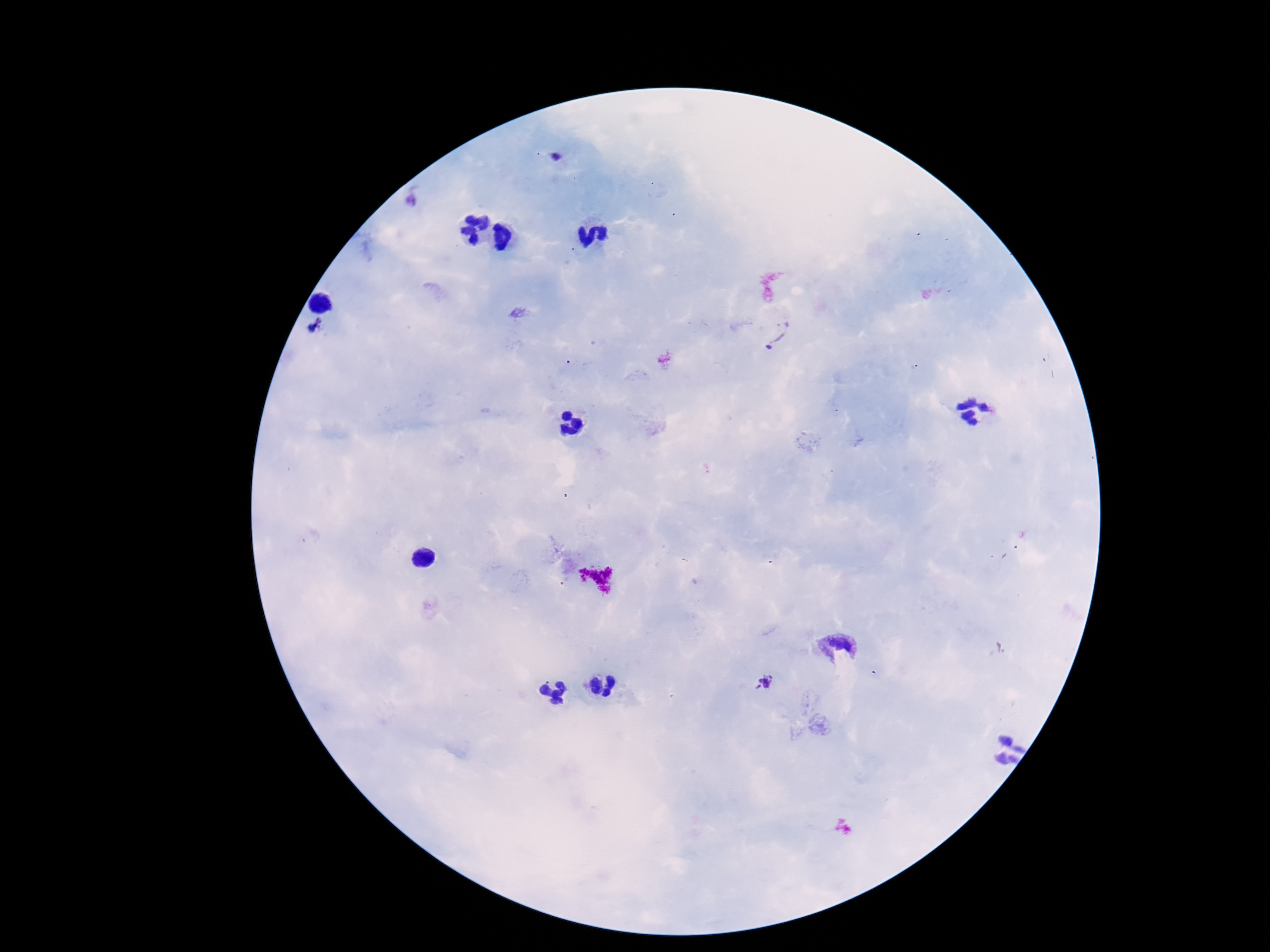

Approximate centers as {x, y} in pixels.
Summary:
  - Plasmodium parasite locations: {316, 324}, {779, 332}, {767, 681}
  - Patient malaria status: infected
  - Capture: smartphone camera through the microscope eyepiece
  - Field of view: single
  - Magnification: 100x
  - Stain: Giemsa
  - Image size: 1270×952 pixels
  - Preparation: thick blood film